Assess this cell for malaria.
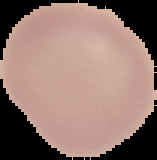
It is uninfected.

From a thin blood film. Cell region segmented out of the field of view; the surrounding area is masked to black. Image is 157×160 pixels.